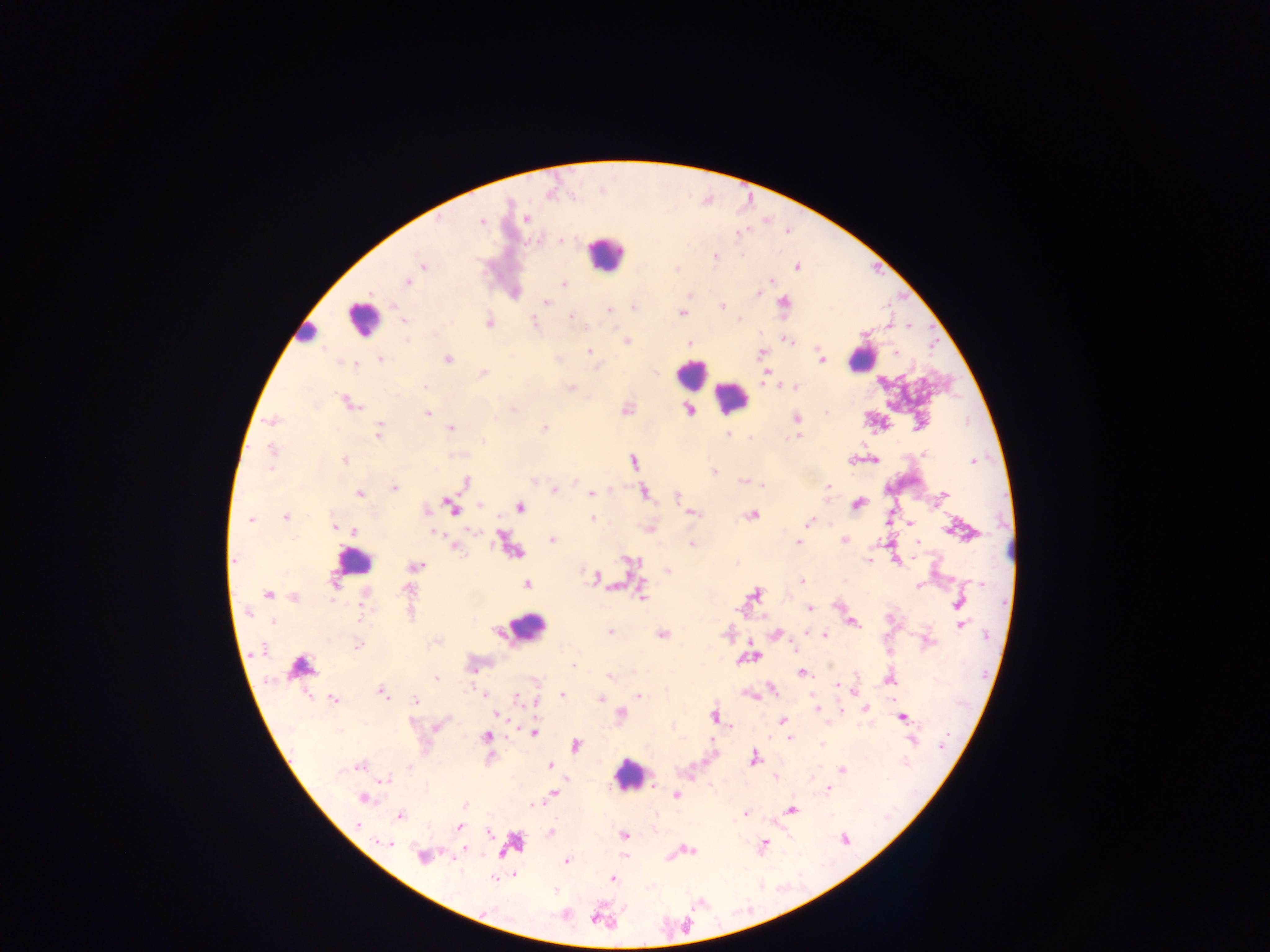

Approximate centers as x y in pixels.
Summary:
  - Malaria parasite locations: 527 219; 481 221; 560 240; 715 256; 423 265; 796 267; 676 269; 770 280; 407 282; 564 284; 757 293; 546 302; 783 302; 721 306; 633 307; 609 310; 682 314; 571 316; 739 318; 404 319; 533 322; 489 323; 586 326; 626 340; 788 340; 689 343; 589 351; 761 353; 896 353; 380 358; 448 358; 821 360; 353 364; 484 373; 767 375; 425 387; 572 388; 795 388; 350 404; 513 409; 689 411; 427 413; 797 418; 272 421; 451 428; 543 428; 378 432; 727 434; 796 436; 749 437; 483 441; 271 449; 924 453; 345 460; 875 460; 973 461; 633 463; 271 470; 714 472; 465 482; 742 482; 762 485; 828 485; 393 488; 553 491; 645 492; 591 493; 359 494; 945 494; 677 497; 480 505; 452 506; 520 507; 425 509; 693 513; 751 516; 286 517; 593 519; 250 521; 807 523; 911 523; 334 525; 353 531; 434 533; 503 539; 553 540; 845 540; 798 542; 918 543; 692 544; 456 548; 234 559; 868 560; 630 561; 416 566; 668 571; 597 577; 802 581; 335 582; 527 584; 918 586; 408 589; 642 593; 755 594; 268 595; 294 598; 959 602; 810 608; 361 611; 272 622; 854 623; 962 624; 610 632; 806 633; 662 635; 825 636; 358 646; 263 649; 299 666; 573 666; 472 670; 803 672; 609 677; 437 679; 889 679; 836 684; 772 690; 854 691; 382 693; 484 695; 562 695; 638 696; 333 698; 518 698; 600 699; 416 700; 865 708; 818 709; 621 713; 497 715; 714 716; 903 718; 782 721; 438 726; 339 731; 534 733; 485 736; 790 738; 822 744; 576 745; 754 758; 359 766; 550 766; 410 767; 842 769; 340 771; 775 777; 386 780; 828 789; 553 794; 677 795; 363 799; 464 805; 534 807; 792 809; 745 813; 400 816; 358 825; 459 827; 550 832; 490 834; 624 835; 845 839; 386 843; 764 843; 464 849; 691 850; 422 856; 567 860; 514 875; 494 878; 613 878; 484 911
  - Leukocyte locations: 606 253; 361 317; 306 335; 861 359; 692 375; 732 397; 353 559; 526 629; 629 775
  - Country: Ghana
  - Capture: mobile-phone photograph through a microscope
  - Field of view: single
  - Image size: 1270×952 pixels
  - Preparation: thick blood smear